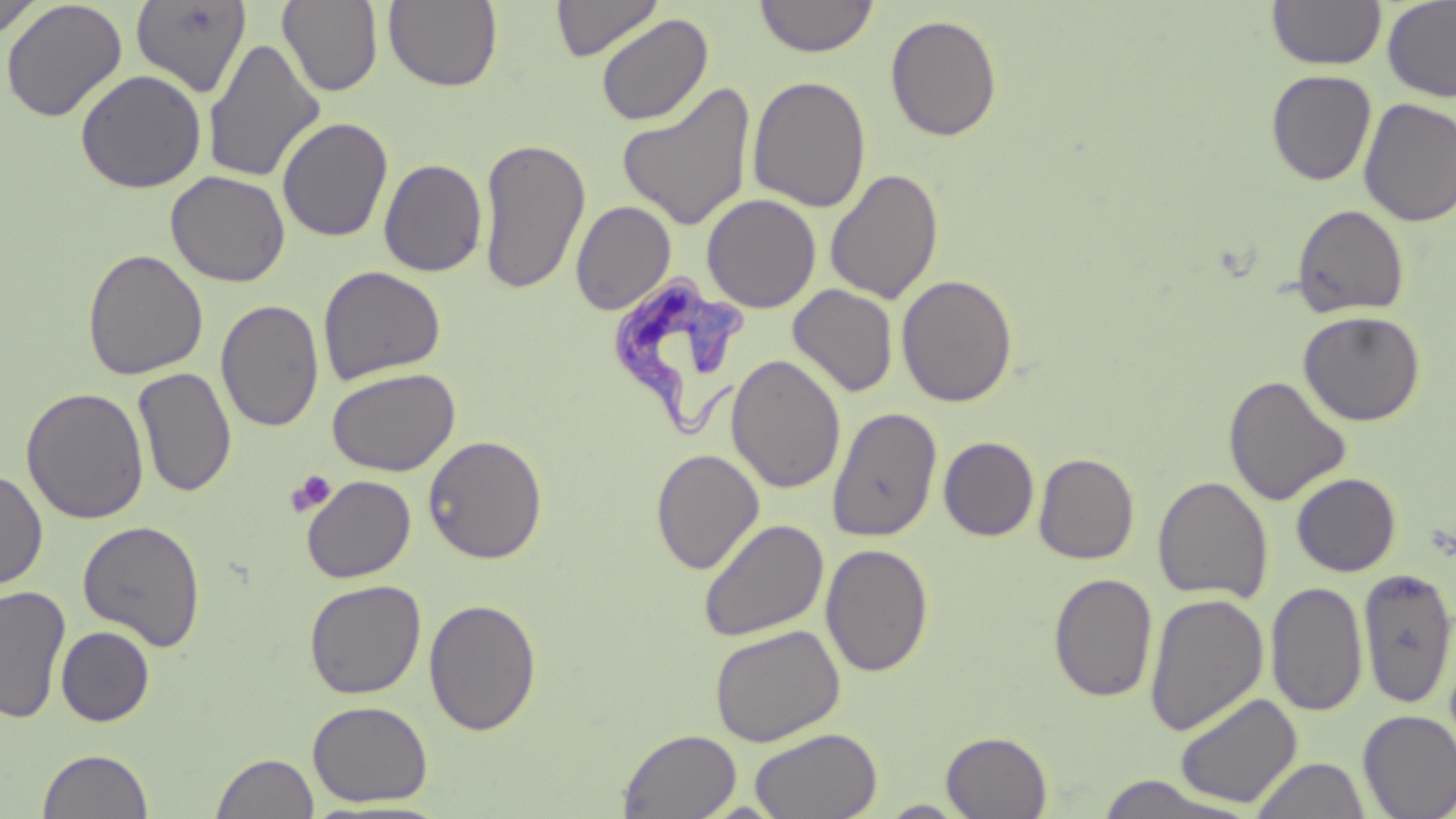

Summary:
  - Coordinate format: approximate bounding boxes as named x1/y1/x2/y2 corners in pixels
  - Trypanosoma brucei locations: (x1=604, y1=271, x2=754, y2=440)
  - Platelet locations: (x1=286, y1=470, x2=336, y2=517)
  - Uninfected red blood cell locations: (x1=0, y1=0, x2=43, y2=40), (x1=1, y1=0, x2=127, y2=123), (x1=551, y1=0, x2=663, y2=62), (x1=755, y1=0, x2=878, y2=58), (x1=1383, y1=0, x2=1456, y2=103), (x1=130, y1=1, x2=252, y2=98), (x1=277, y1=1, x2=384, y2=97), (x1=383, y1=1, x2=503, y2=91), (x1=1267, y1=1, x2=1386, y2=69), (x1=595, y1=13, x2=714, y2=126), (x1=885, y1=13, x2=1003, y2=141), (x1=203, y1=38, x2=325, y2=184), (x1=75, y1=69, x2=207, y2=193), (x1=1266, y1=69, x2=1377, y2=186), (x1=747, y1=75, x2=871, y2=213), (x1=617, y1=82, x2=757, y2=231), (x1=1358, y1=97, x2=1456, y2=227), (x1=277, y1=116, x2=393, y2=242), (x1=477, y1=136, x2=591, y2=295), (x1=379, y1=158, x2=488, y2=277), (x1=825, y1=168, x2=944, y2=304), (x1=166, y1=170, x2=290, y2=286), (x1=701, y1=193, x2=821, y2=313), (x1=571, y1=201, x2=676, y2=315), (x1=1292, y1=204, x2=1410, y2=318), (x1=82, y1=248, x2=208, y2=380), (x1=318, y1=265, x2=446, y2=384), (x1=896, y1=274, x2=1018, y2=407), (x1=787, y1=284, x2=898, y2=398), (x1=216, y1=299, x2=325, y2=432), (x1=1298, y1=310, x2=1425, y2=426), (x1=726, y1=353, x2=846, y2=494), (x1=133, y1=366, x2=237, y2=498), (x1=327, y1=367, x2=460, y2=476), (x1=1223, y1=375, x2=1351, y2=506), (x1=21, y1=386, x2=149, y2=524), (x1=828, y1=406, x2=943, y2=542), (x1=423, y1=435, x2=548, y2=564), (x1=938, y1=436, x2=1039, y2=541), (x1=650, y1=448, x2=765, y2=575), (x1=1034, y1=453, x2=1139, y2=564), (x1=0, y1=467, x2=48, y2=590), (x1=1291, y1=472, x2=1401, y2=576), (x1=301, y1=475, x2=416, y2=582), (x1=1153, y1=476, x2=1273, y2=603), (x1=698, y1=518, x2=830, y2=642), (x1=78, y1=519, x2=206, y2=650), (x1=821, y1=543, x2=934, y2=677), (x1=1358, y1=567, x2=1456, y2=709), (x1=1048, y1=573, x2=1158, y2=703), (x1=304, y1=579, x2=426, y2=699), (x1=1266, y1=581, x2=1368, y2=717), (x1=0, y1=584, x2=71, y2=724), (x1=1145, y1=592, x2=1269, y2=736), (x1=423, y1=598, x2=542, y2=736), (x1=709, y1=624, x2=846, y2=746), (x1=56, y1=626, x2=155, y2=726), (x1=1174, y1=691, x2=1302, y2=809), (x1=307, y1=700, x2=433, y2=807), (x1=1358, y1=709, x2=1456, y2=818), (x1=749, y1=727, x2=883, y2=819), (x1=618, y1=728, x2=741, y2=818), (x1=941, y1=730, x2=1053, y2=818), (x1=37, y1=748, x2=153, y2=819), (x1=211, y1=752, x2=319, y2=819), (x1=1251, y1=756, x2=1370, y2=819), (x1=1093, y1=774, x2=1250, y2=818), (x1=877, y1=800, x2=973, y2=817)
  - Slide-level diagnosis: Trypanosoma brucei
  - Modality: optical microscopy
  - Stain: May-Grünwald-Giemsa
  - Field of view: single
  - Preparation: thin blood film
  - Image size: 1456×819 pixels
  - Magnification: 1000x